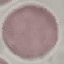

Result: no malaria parasites detected. Automatically extracted cell patch, resized to 64 × 64 pixels. Thin blood film. Acquired by smartphone through the microscope eyepiece. Giemsa-stained preparation.